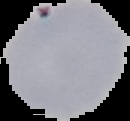

image type = cell region segmented out of the field of view; surrounding area masked to black
preparation = thin blood smear
image size = 130×121 pixels
malaria status = parasitized